Assess this cell for malaria.
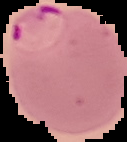

It is parasitized.

Summary:
  - Image type: segmented cell region with the area outside set to black
  - Image size: 127×142 pixels
  - Preparation: thin blood film